Assess the morphology of the erythrocytes.
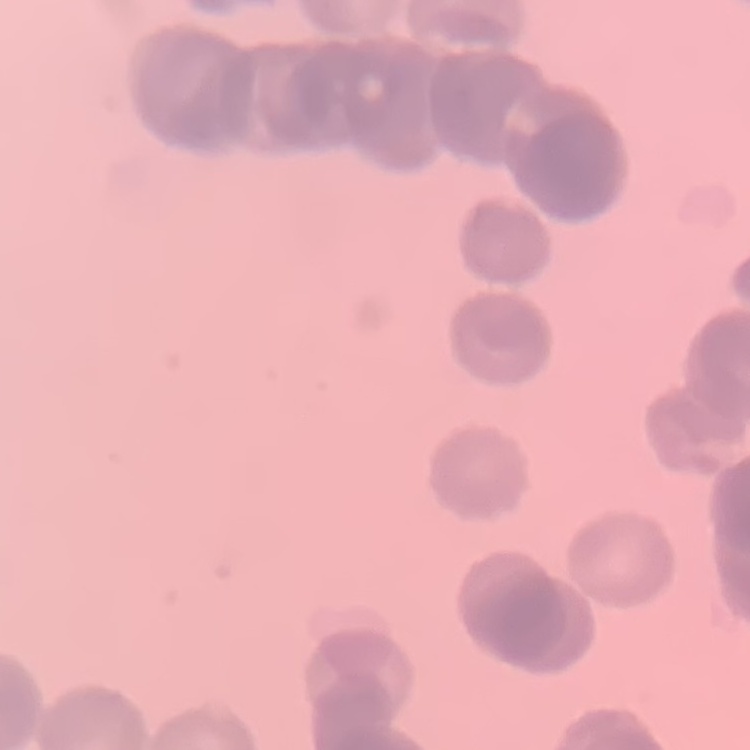

They show rouleaux formation.

Summary:
  - Preparation: thin blood smear
  - Stain: Field's or Giemsa
  - Image type: one tile cut from a larger photomicrograph